Assess the morphology of the red blood cells.
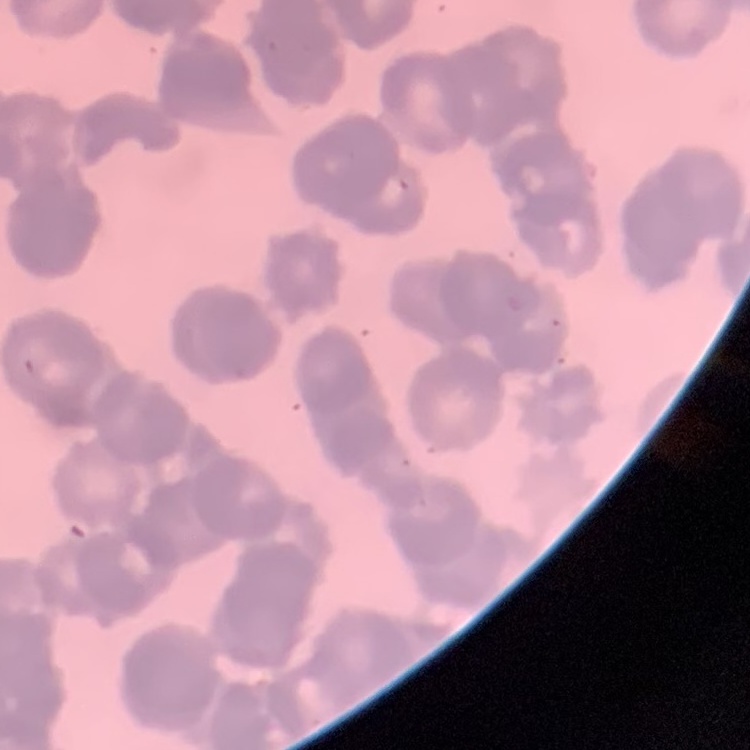

They show rouleaux formation.

Summary:
  - Preparation: thin peripheral smear
  - Image type: one tile cut from a larger photomicrograph
  - Stain: Field's or Giemsa